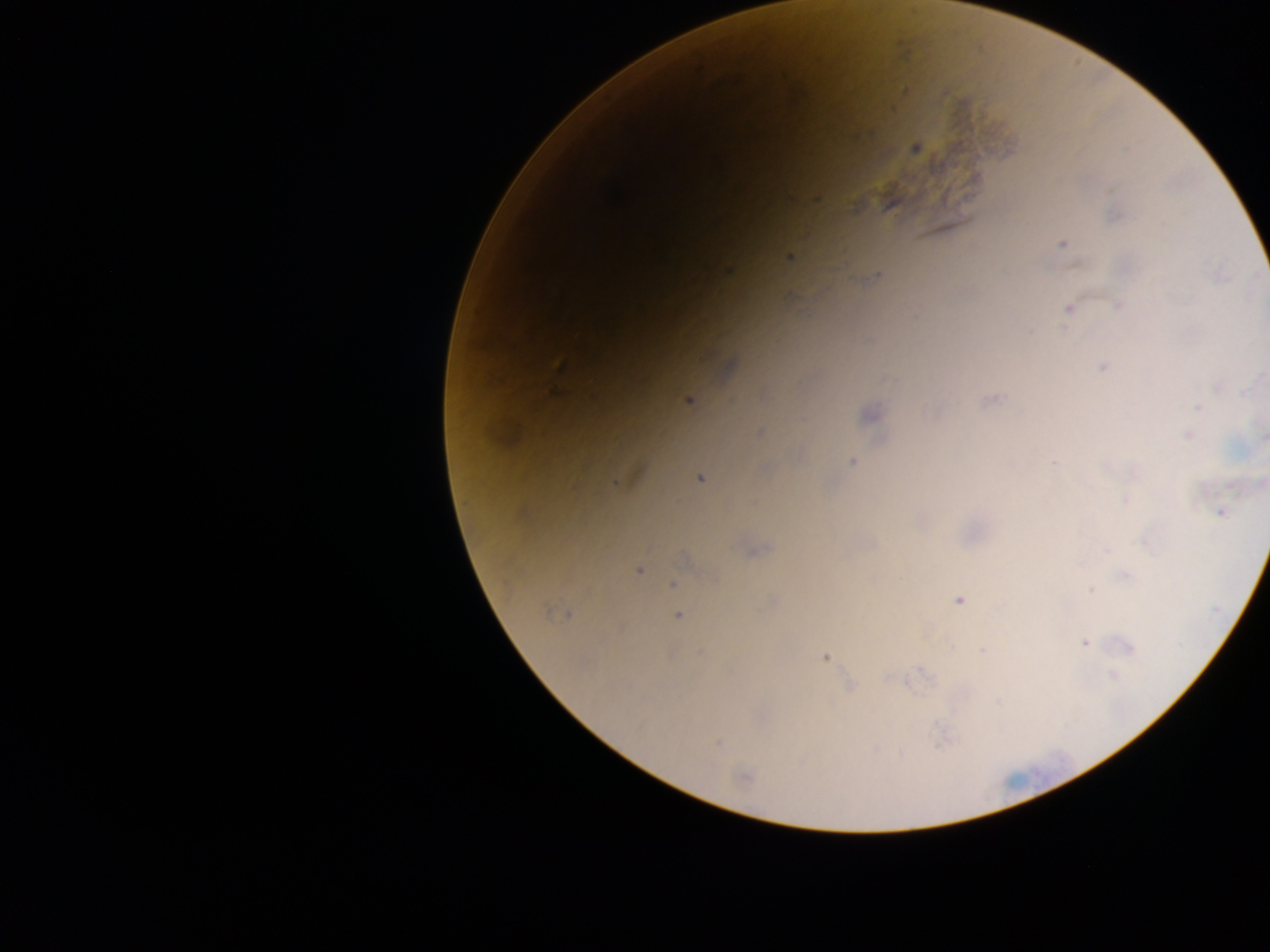 Approximate centers as x y in pixels. Plasmodium parasite locations: 1108 192; 1062 243; 789 260; 1067 307; 1101 367; 1216 388; 988 400; 685 402; 1197 407; 866 412; 1186 435; 851 461; 1052 464; 1219 511; 1105 550; 1128 576; 1092 589; 1086 643; 1133 648; 824 658; 1113 676; 717 742; 941 746. Mobile-phone photograph taken through the microscope. Image is 1270×952 pixels. One field of view. Thick blood smear. Collected in Ghana.